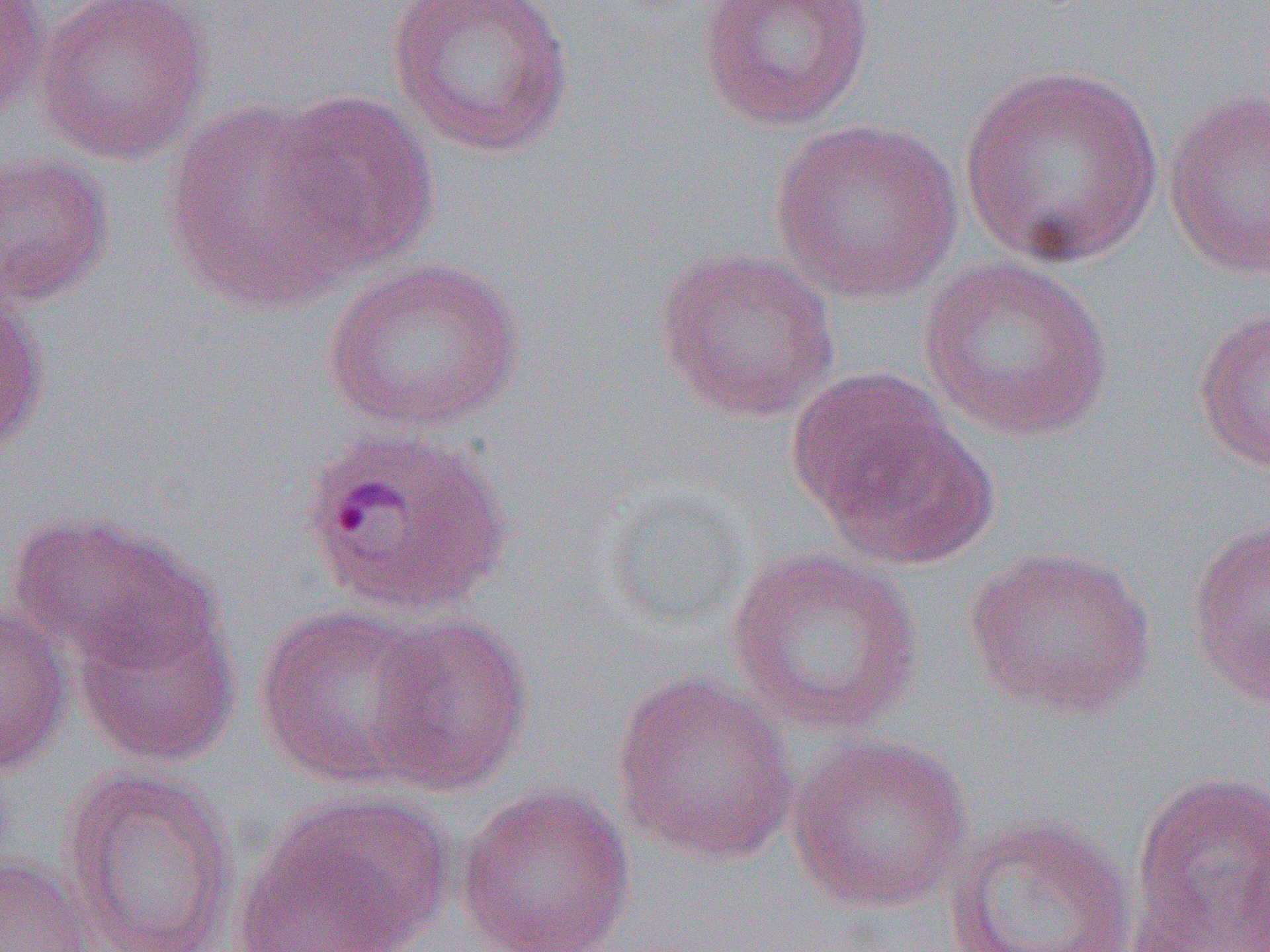 Approximate bounding boxes as [x1, y1, x2, y2] in pixels. Plasmodium ovale-infected red blood cell locations: [298, 424, 516, 619]. Uninfected red blood cell locations: [30, 0, 213, 166], [385, 0, 576, 159], [697, 0, 876, 131], [0, 1, 47, 123], [957, 65, 1165, 270], [1163, 87, 1270, 280], [268, 90, 439, 271], [162, 99, 364, 314], [770, 118, 963, 303], [0, 151, 114, 309], [651, 246, 842, 423], [918, 255, 1113, 442], [321, 257, 525, 435], [0, 285, 48, 458], [1193, 304, 1270, 474], [787, 367, 973, 549], [601, 488, 753, 635], [6, 508, 213, 670], [1185, 516, 1270, 707], [962, 545, 1157, 719], [725, 547, 926, 737], [71, 600, 241, 767], [0, 601, 72, 779], [255, 604, 446, 792], [365, 614, 535, 797], [610, 671, 800, 866], [786, 734, 973, 914], [59, 766, 238, 952], [1129, 770, 1269, 950], [454, 782, 637, 952], [234, 789, 453, 952], [944, 813, 1139, 952], [1236, 820, 1270, 952], [0, 852, 96, 951]. Slide-level diagnosis: Plasmodium ovale. 1000x magnification. Image is 1270×952 pixels. Light microscopy. Thin blood smear. Single field of view.